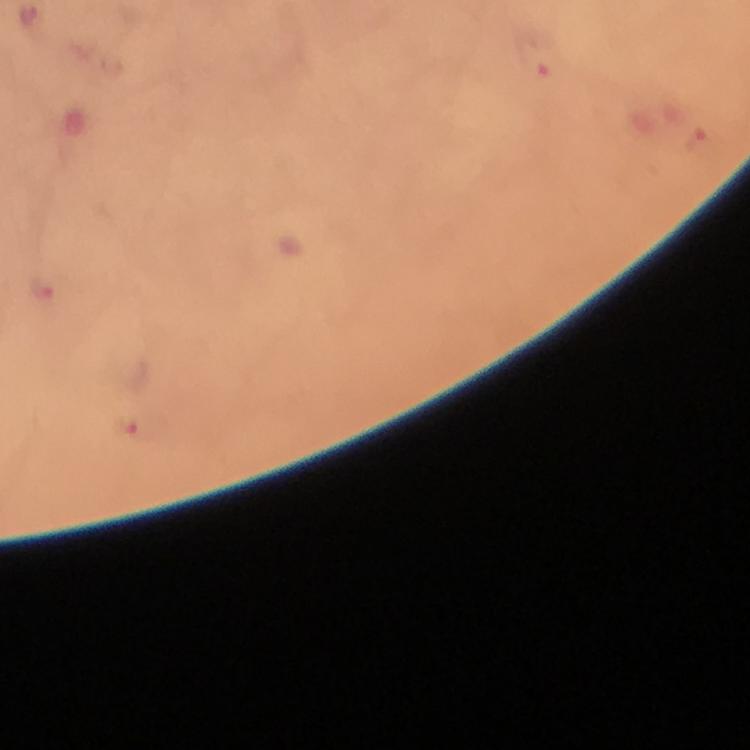

magnification = 100x
stain = Giemsa
capture = smartphone mounted on the microscope
context = from a diagnostic examination for malaria
image size = 750×750 pixels
Plasmodium parasite locations = approximate object centers, in pixels from the top-left corner: (x=534, y=63), (x=700, y=139), (x=131, y=426)
immersion oil = applied
cropped from = one field of view
preparation = thick blood film